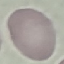 Malaria status: uninfected. Thin smear of blood. Photographed with a smartphone camera at the microscope eyepiece. Giemsa-stained preparation. Automatically extracted cell patch, resized to 64 × 64 pixels.